Name the cell type shown.
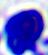
A leukocyte.

Captured at 400x magnification. Micrograph.